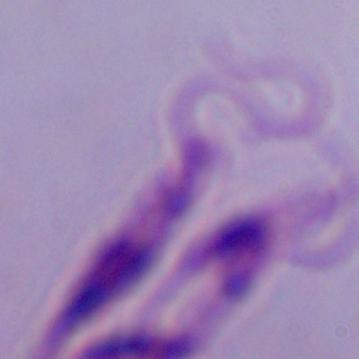
{
  "identification": "Leishmania",
  "modality": "photomicrograph",
  "magnification": "1000x"
}